Name the blood parasite species.
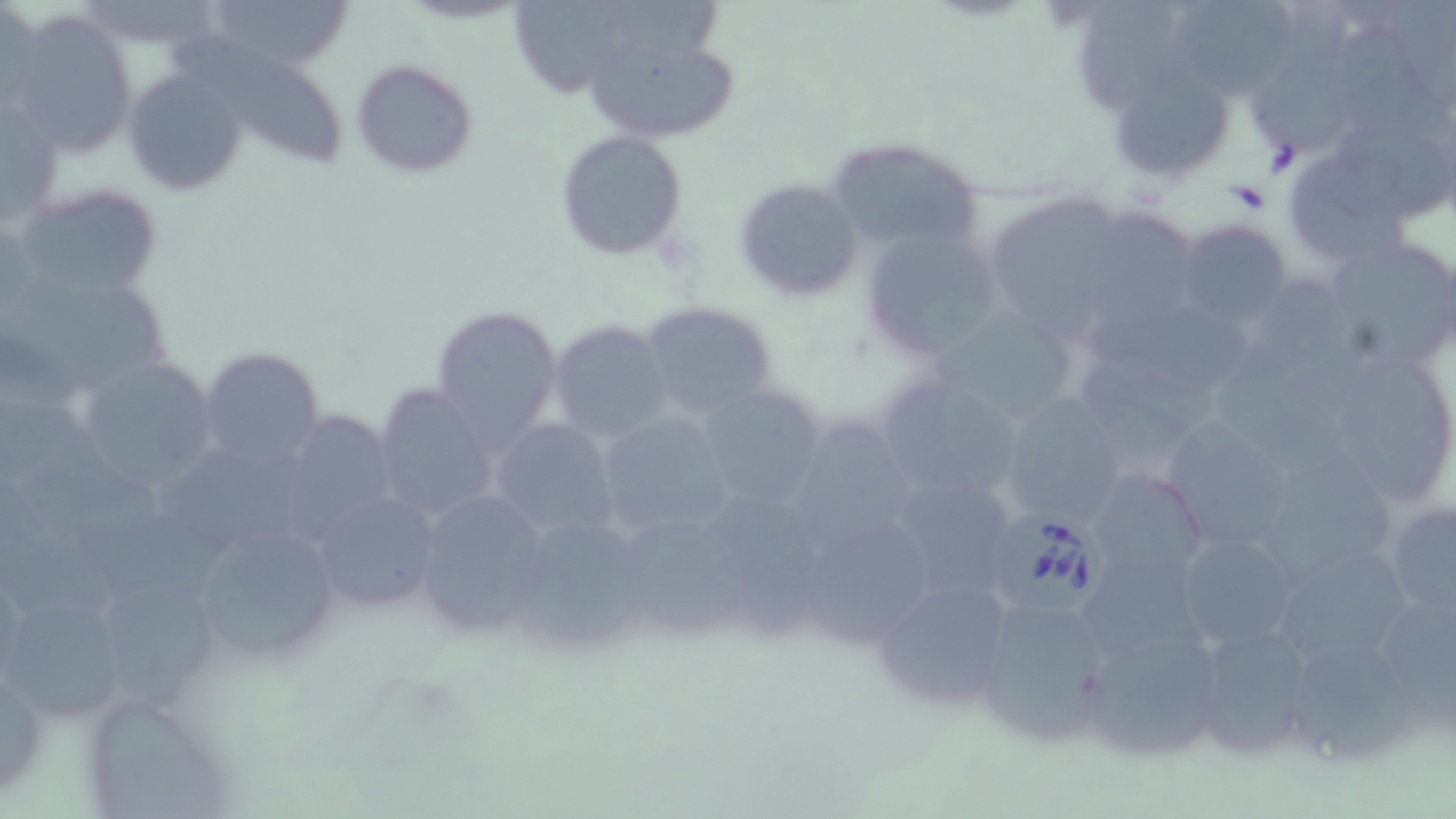
Babesia divergens.

Approximate bounding boxes as named x1/y1/x2/y2 corners in pixels. Uninfected red blood cell locations: (x1=204, y1=0, x2=353, y2=72), (x1=1079, y1=0, x2=1178, y2=114), (x1=1253, y1=0, x2=1356, y2=162), (x1=509, y1=1, x2=633, y2=99), (x1=604, y1=1, x2=728, y2=65), (x1=1177, y1=3, x2=1295, y2=98), (x1=8, y1=12, x2=139, y2=157), (x1=581, y1=20, x2=742, y2=149), (x1=1336, y1=28, x2=1451, y2=152), (x1=171, y1=31, x2=351, y2=169), (x1=351, y1=58, x2=477, y2=177), (x1=119, y1=66, x2=248, y2=197), (x1=1107, y1=66, x2=1239, y2=185), (x1=1, y1=95, x2=61, y2=230), (x1=1338, y1=127, x2=1453, y2=221), (x1=555, y1=131, x2=689, y2=261), (x1=823, y1=136, x2=989, y2=256), (x1=1293, y1=158, x2=1415, y2=265), (x1=734, y1=178, x2=863, y2=300), (x1=10, y1=183, x2=164, y2=303), (x1=989, y1=195, x2=1115, y2=344), (x1=1097, y1=208, x2=1198, y2=329), (x1=1173, y1=220, x2=1292, y2=326), (x1=862, y1=226, x2=1007, y2=360), (x1=1331, y1=243, x2=1453, y2=365), (x1=15, y1=277, x2=171, y2=393), (x1=1086, y1=300, x2=1254, y2=391), (x1=639, y1=302, x2=779, y2=421), (x1=431, y1=305, x2=564, y2=446), (x1=934, y1=306, x2=1085, y2=426), (x1=548, y1=320, x2=673, y2=443), (x1=390, y1=334, x2=540, y2=485), (x1=1213, y1=341, x2=1355, y2=478), (x1=197, y1=347, x2=327, y2=468), (x1=1340, y1=355, x2=1443, y2=498), (x1=1073, y1=360, x2=1224, y2=463), (x1=84, y1=361, x2=216, y2=494), (x1=871, y1=372, x2=1029, y2=505), (x1=692, y1=380, x2=833, y2=510), (x1=371, y1=382, x2=503, y2=522), (x1=997, y1=392, x2=1129, y2=529), (x1=592, y1=409, x2=742, y2=541), (x1=289, y1=410, x2=395, y2=542), (x1=1160, y1=417, x2=1300, y2=555), (x1=490, y1=418, x2=621, y2=538), (x1=796, y1=421, x2=915, y2=555), (x1=17, y1=430, x2=167, y2=543), (x1=163, y1=449, x2=310, y2=547), (x1=1271, y1=452, x2=1397, y2=576), (x1=1086, y1=466, x2=1210, y2=587), (x1=881, y1=469, x2=1024, y2=604), (x1=0, y1=479, x2=124, y2=622), (x1=306, y1=488, x2=445, y2=611), (x1=410, y1=488, x2=556, y2=635), (x1=714, y1=495, x2=826, y2=638), (x1=1380, y1=496, x2=1456, y2=631), (x1=80, y1=511, x2=234, y2=606), (x1=631, y1=522, x2=746, y2=634), (x1=802, y1=522, x2=931, y2=644), (x1=519, y1=526, x2=642, y2=648), (x1=207, y1=530, x2=333, y2=660), (x1=1171, y1=531, x2=1305, y2=650), (x1=1284, y1=549, x2=1416, y2=655), (x1=1086, y1=559, x2=1209, y2=662), (x1=870, y1=573, x2=1018, y2=709), (x1=107, y1=582, x2=220, y2=709), (x1=973, y1=593, x2=1115, y2=747), (x1=1, y1=598, x2=119, y2=722), (x1=1380, y1=607, x2=1456, y2=727), (x1=1075, y1=614, x2=1230, y2=764), (x1=1190, y1=621, x2=1321, y2=755), (x1=1296, y1=646, x2=1416, y2=757), (x1=0, y1=647, x2=47, y2=804), (x1=95, y1=705, x2=234, y2=819). Babesia divergens-infected red blood cell locations: (x1=997, y1=507, x2=1114, y2=617). May-Grünwald-Giemsa-stained preparation. 1000x magnification. Light microscopy. Thin blood smear. Image is 1456×819 pixels. Single field of view.